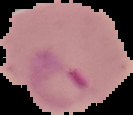
Segmented cell region on a black background. Image is 133×115 pixels. From a thin blood smear. Result: Plasmodium parasites identified.